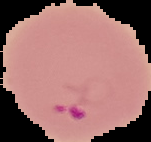
preparation = thin blood smear
image size = 151×142 pixels
result = Plasmodium parasites identified
image type = segmented cell region on a black background